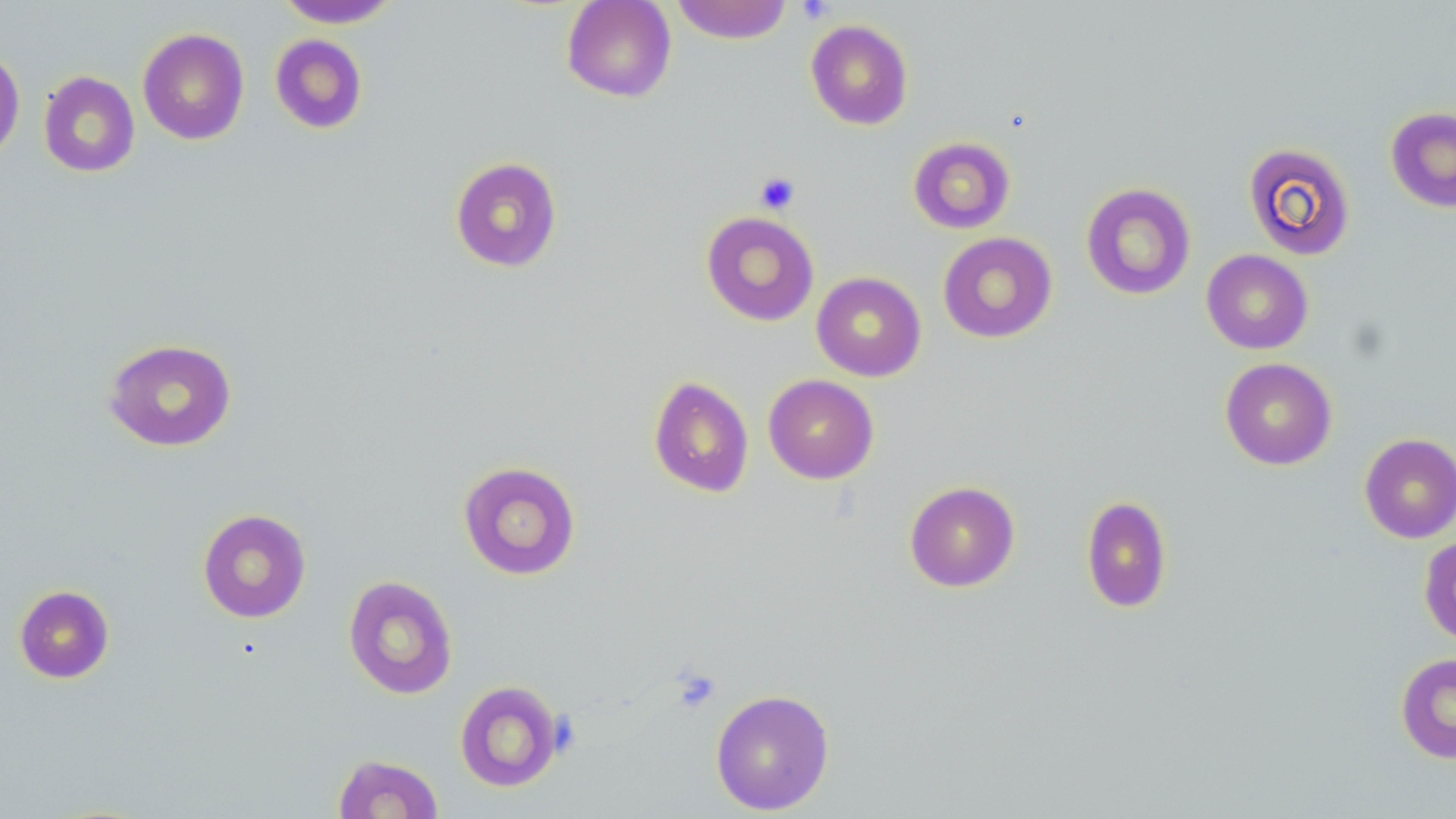
{
  "slide_level_diagnosis": "negative for blood parasites",
  "field_of_view": "single",
  "preparation": "thin blood film",
  "modality": "light microscopy",
  "magnification": "1000x",
  "image_size": "1456×819 pixels",
  "uninfected_red_blood_cell_locations": "approximate bounding boxes as (x1, y1, x2, y2) in pixels: (275, 0, 402, 28), (561, 0, 677, 102), (671, 0, 794, 44), (805, 19, 914, 130), (137, 28, 249, 145), (269, 33, 368, 134), (0, 47, 25, 163), (38, 71, 140, 178), (1385, 106, 1456, 213), (908, 136, 1016, 234), (1243, 142, 1356, 261), (449, 156, 563, 273), (1080, 182, 1197, 300), (701, 211, 820, 326), (938, 232, 1058, 343), (1201, 249, 1314, 354), (811, 271, 926, 381), (103, 338, 238, 452), (1220, 357, 1337, 470), (763, 374, 879, 484), (648, 375, 754, 498), (1358, 433, 1456, 543), (457, 461, 581, 580), (904, 480, 1020, 592), (1080, 495, 1172, 613), (197, 509, 311, 623), (1418, 535, 1456, 647), (343, 575, 459, 699), (13, 584, 114, 683), (1395, 652, 1456, 764), (454, 680, 564, 792), (710, 689, 835, 815), (332, 753, 444, 818)",
  "platelet_locations": "approximate bounding boxes as (x1, y1, x2, y2) in pixels: (796, 0, 836, 24), (754, 171, 801, 215)",
  "stain": "May-Grünwald-Giemsa"
}